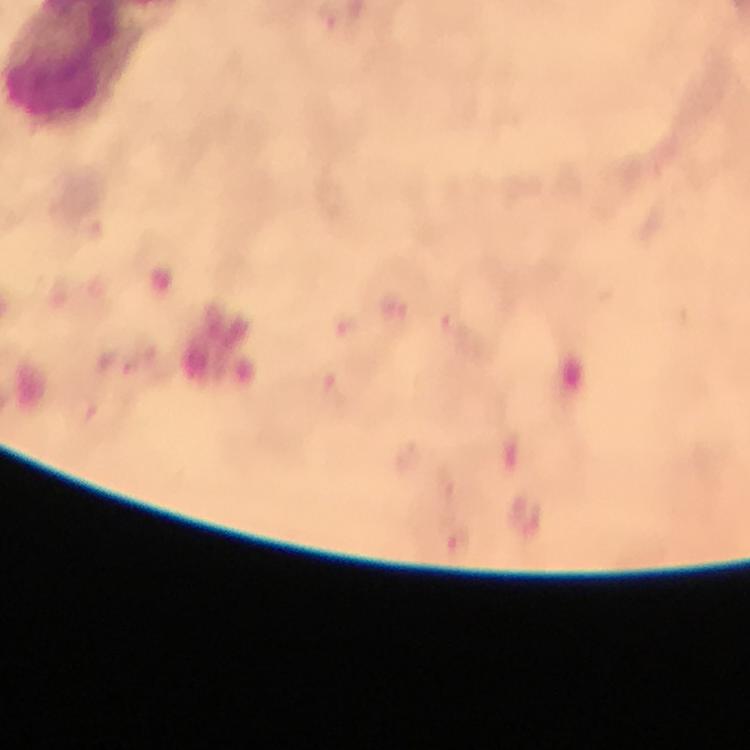

{
  "malaria_parasite_locations": "approximate centers as [x, y] in pixels: [456, 546]",
  "stain": "Giemsa",
  "image_size": "750×750 pixels",
  "preparation": "thick blood smear",
  "magnification": "100x",
  "capture": "smartphone mounted on the microscope",
  "context": "from a diagnostic examination for malaria",
  "cropped_from": "a single field of view",
  "immersion_oil": "used"
}